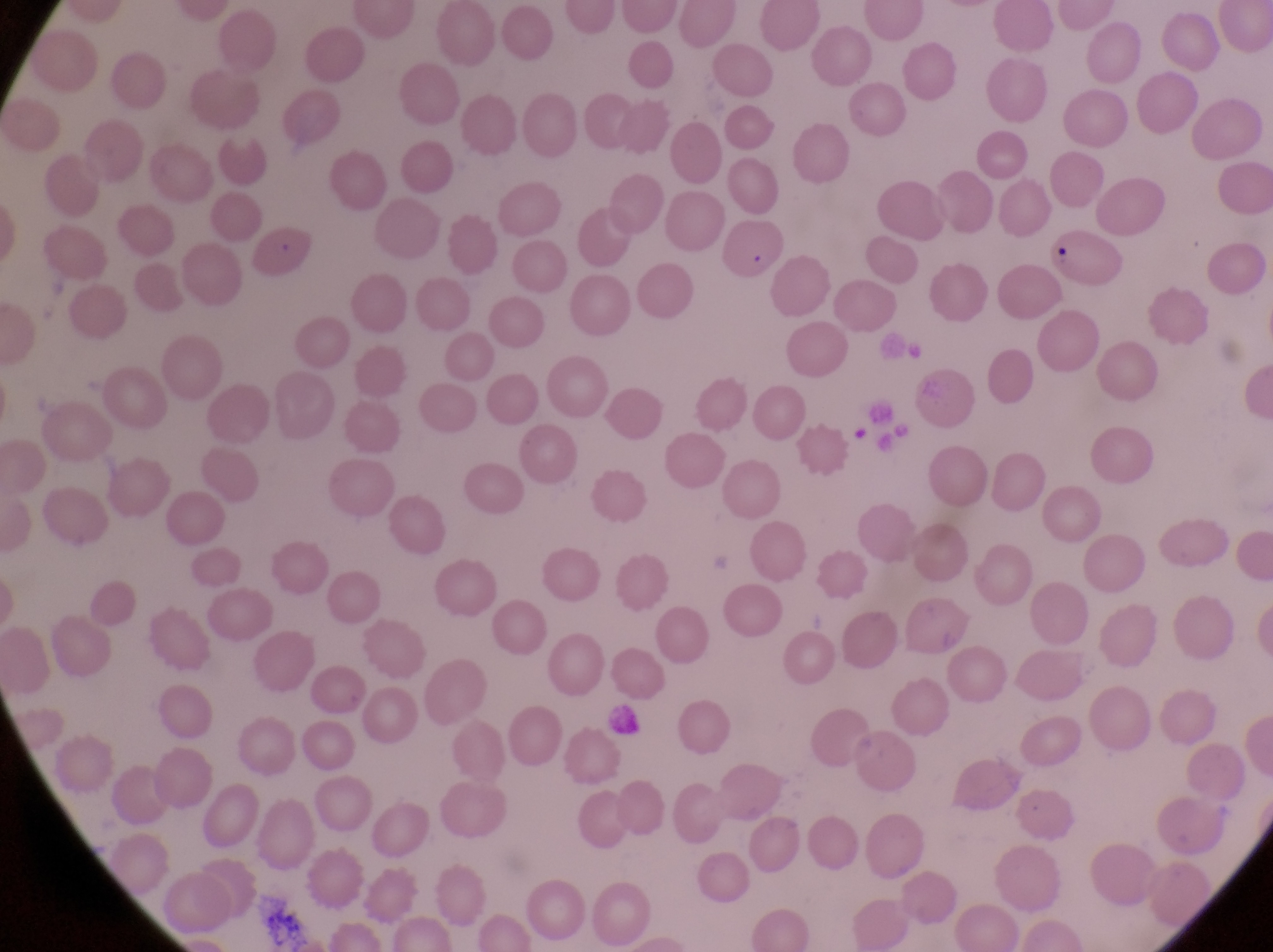 Approximate bounding boxes as (left, top, right, bottom) in pixels. Parasitised red blood cell locations: (250, 217, 324, 284), (1043, 229, 1119, 284). Collected in Uganda. At a magnification of 1000x. Thin blood smear. Single field of view. Image is 1273×952 pixels. Photographed through the eyepiece of an Olympus CX-23 microscope with a smartphone camera.